Evaluate for malaria.
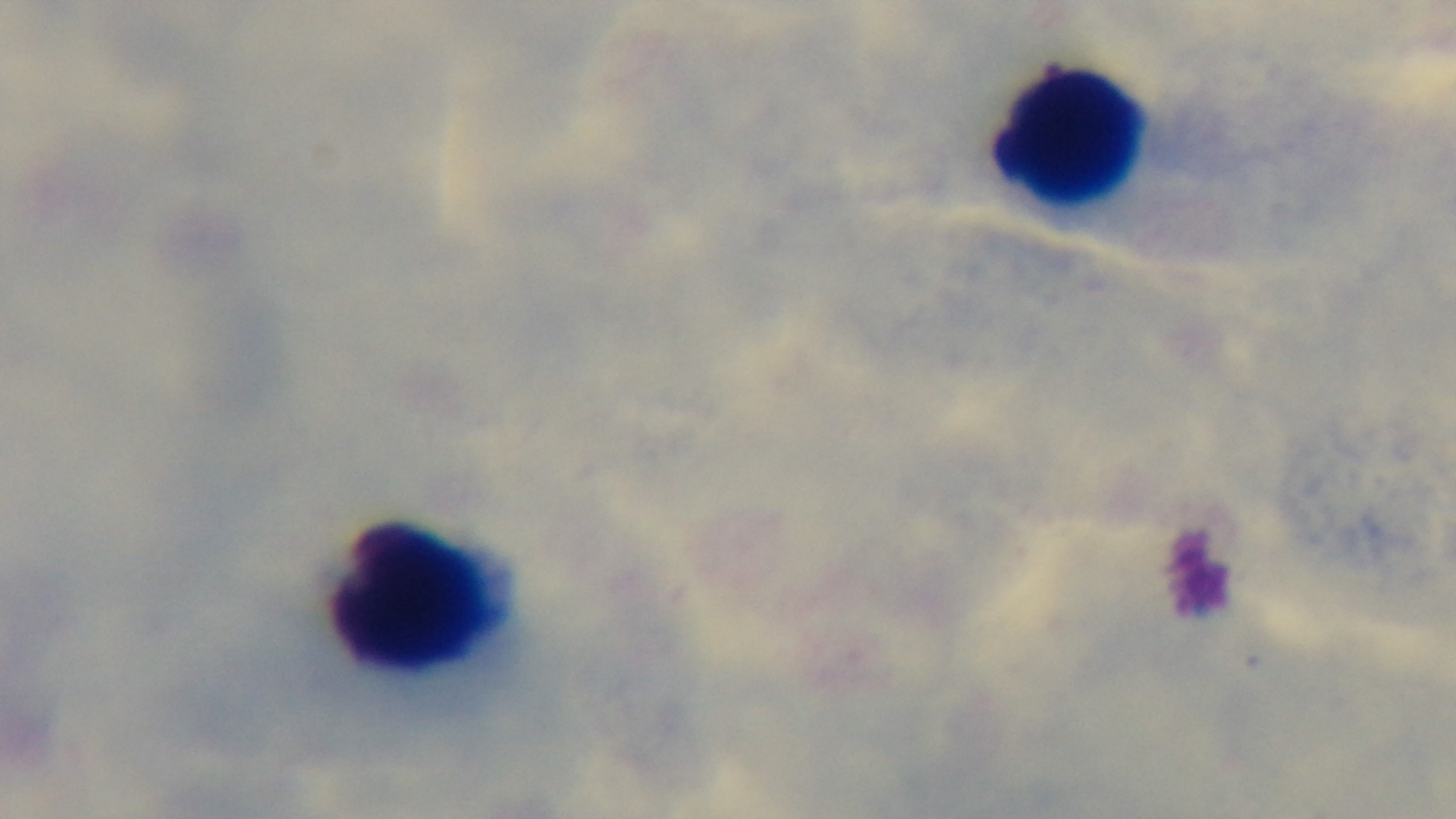
It is uninfected.

{
  "stain": "Giemsa",
  "modality": "light microscopy",
  "field_of_view": "one from the slide",
  "preparation": "thick smear",
  "capture": "mounted 4K digital camera",
  "objective": "100x oil immersion"
}